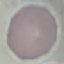

malaria status = uninfected
capture = smartphone through the microscope eyepiece
preparation = thin smear
image type = automatically extracted cell patch, resized to 64 × 64 pixels
stain = Giemsa